Report the malaria status of this cell.
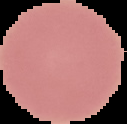

Uninfected.

Image is 127×124 pixels. From a thin blood film. Segmented cell region on a black background.